Locate every Plasmodium malariae-infected red blood cell.
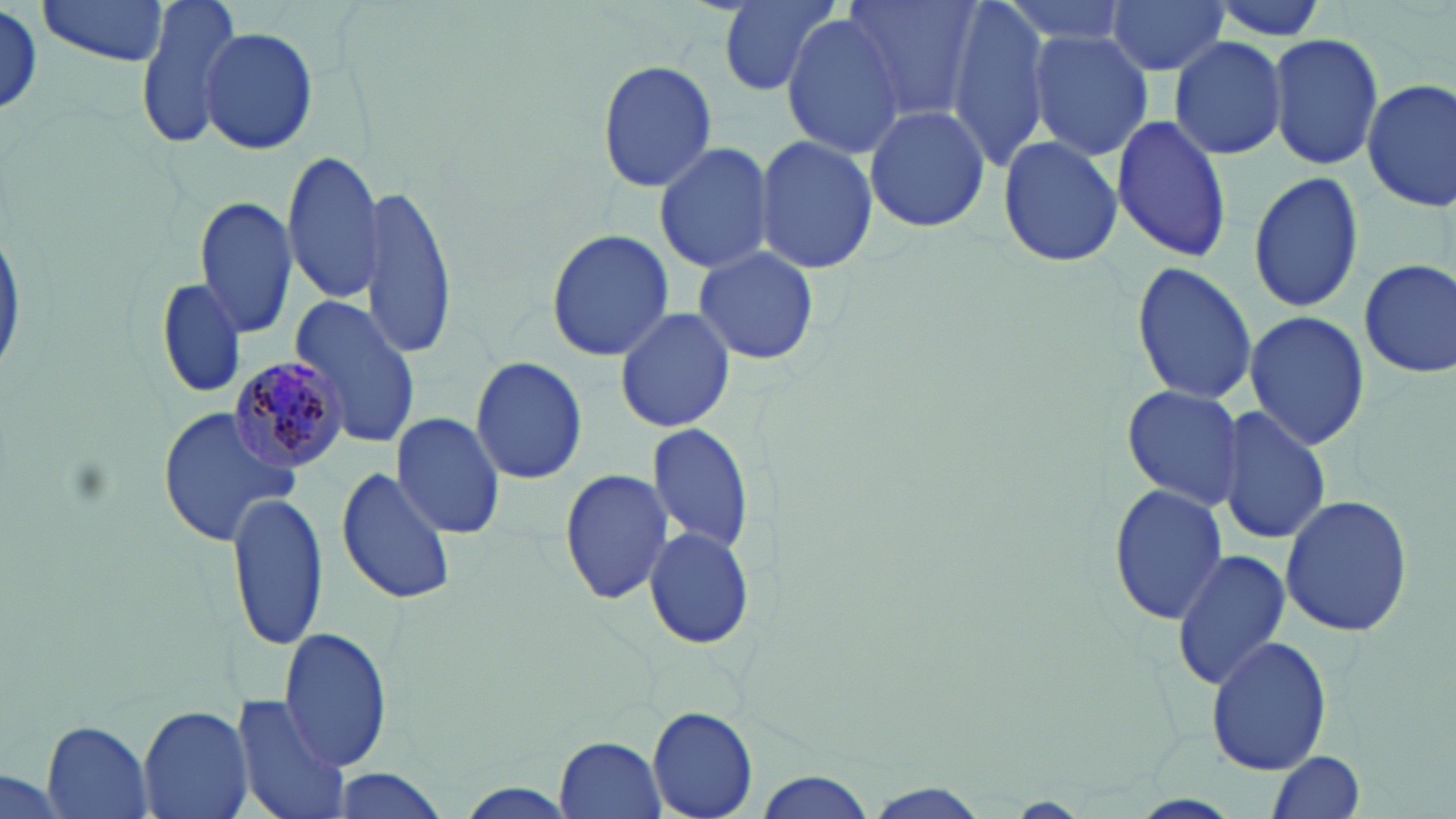
Approximate bounding boxes as (x1, y1, x2, y2) in pixels.
Plasmodium malariae-infected red blood cells: (225, 356, 350, 475).

slide-level diagnosis = Plasmodium malariae
field of view = single
preparation = thin blood smear
stain = May-Grünwald-Giemsa
modality = light microscopy
image size = 1456×819 pixels
uninfected red blood cell locations = approximate bounding boxes as (x1, y1, x2, y2) in pixels: (35, 0, 174, 67), (132, 0, 244, 150), (710, 0, 845, 98), (841, 0, 986, 121), (946, 0, 1051, 171), (997, 0, 1137, 49), (1106, 0, 1229, 77), (1201, 0, 1332, 44), (0, 8, 45, 113), (780, 12, 907, 159), (198, 26, 318, 155), (1028, 29, 1155, 161), (1270, 32, 1384, 172), (1168, 34, 1288, 160), (595, 58, 718, 192), (1361, 77, 1456, 213), (860, 101, 992, 234), (1111, 114, 1233, 261), (754, 134, 878, 275), (996, 134, 1125, 268), (651, 138, 775, 276), (280, 149, 385, 304), (1246, 170, 1365, 312), (359, 182, 460, 359), (193, 196, 297, 342), (545, 229, 673, 361), (692, 245, 819, 366), (1358, 256, 1456, 378), (1131, 261, 1258, 405), (157, 276, 247, 399), (287, 293, 424, 452), (613, 306, 735, 432), (1244, 309, 1368, 450), (470, 355, 588, 487), (1120, 385, 1245, 510), (158, 404, 299, 545), (1217, 405, 1328, 545), (391, 412, 507, 539), (644, 420, 755, 556), (336, 464, 456, 607), (558, 466, 674, 606), (1108, 484, 1230, 624), (226, 491, 329, 652), (1279, 492, 1413, 638), (642, 522, 757, 648), (1170, 548, 1290, 689), (281, 627, 394, 772), (1206, 636, 1332, 775), (232, 693, 352, 819), (136, 705, 255, 819), (646, 706, 758, 819), (41, 721, 154, 819), (554, 733, 666, 816), (1264, 751, 1365, 819), (0, 768, 71, 819), (327, 769, 455, 819), (750, 769, 878, 818), (857, 780, 994, 819)
magnification = 1000x